Locate every malaria parasite.
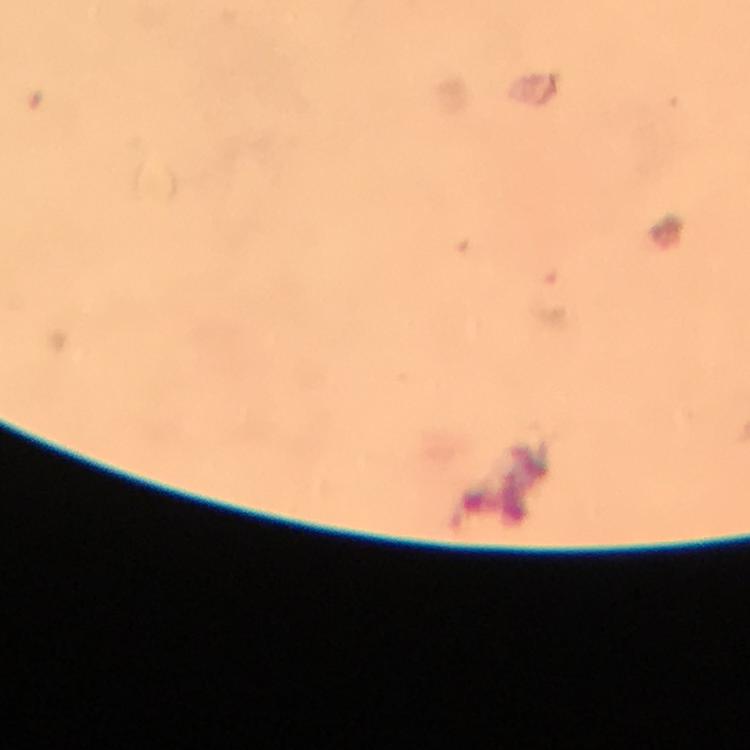

Approximate centers as {x, y} in pixels.
Malaria parasites: {549, 296}.

{
  "capture": "smartphone mounted on the microscope",
  "magnification": "100x",
  "context": "from a malaria diagnostic workup",
  "image_size": "750×750 pixels",
  "stain": "Giemsa",
  "preparation": "thick blood smear",
  "immersion_oil": "applied",
  "cropped_from": "a single field of view"
}